Comment on the morphology of the red blood cells.
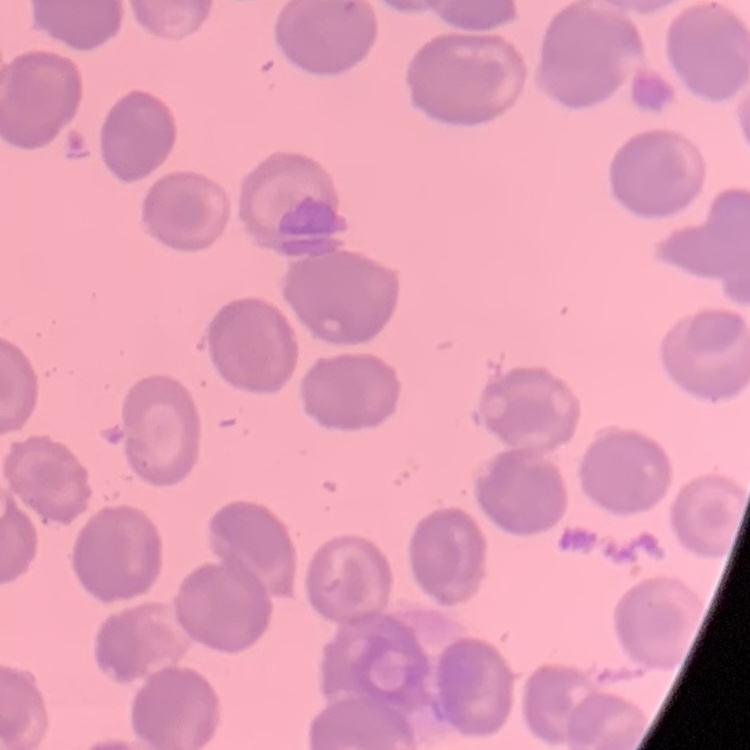
They show no rouleaux formation.

Summary:
  - Image type: one tile cut from a larger photomicrograph
  - Preparation: thin peripheral smear
  - Stain: Field's or Giemsa